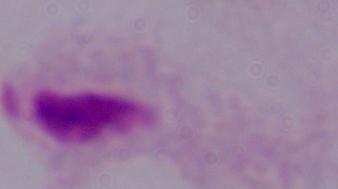
A trichomonad is shown. Micrograph. 1000x magnification.